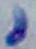
magnification = 1000x
identification = Toxoplasma gondii
modality = photomicrograph